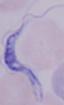

A trypanosome is seen. Captured at 1000x magnification. Micrograph.